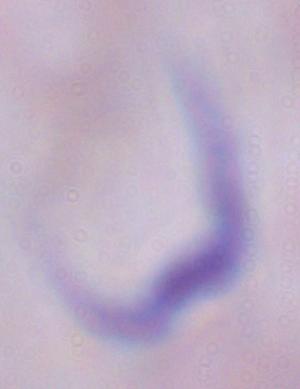

A trypanosome is seen. 1000x magnification. Micrograph.